Describe the morphology of the erythrocytes.
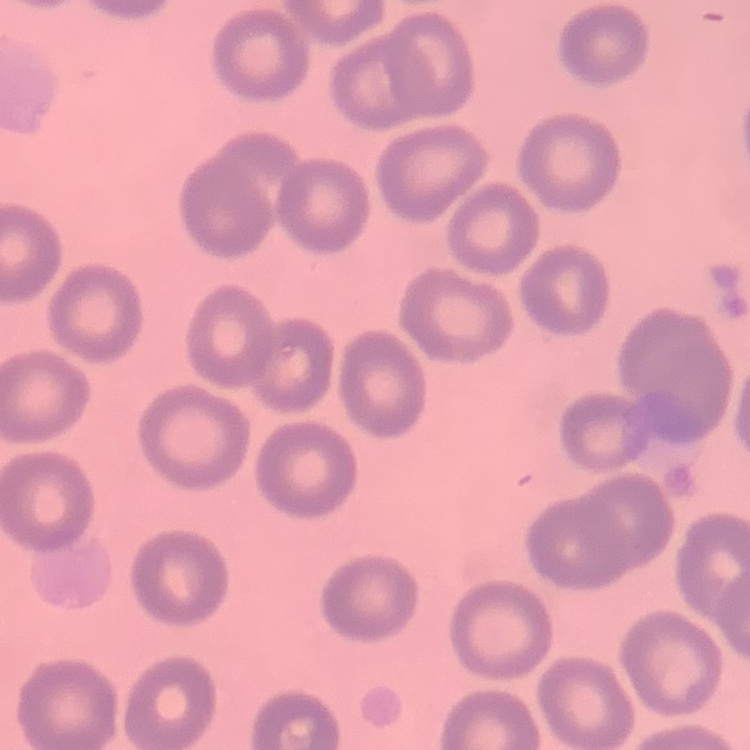

No rouleaux formation.

preparation: thin blood film
image_type: square crop of a larger photomicrograph
stain: Field's or Giemsa